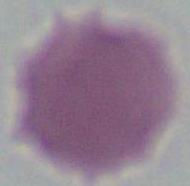

magnification = 1000x
identification = erythrocyte
modality = photomicrograph